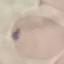 Result: negative for malaria parasites. Automatically extracted cell patch, resized to 64 × 64 pixels. Thin smear of blood. Giemsa stain. Acquired by smartphone through the microscope eyepiece.